Outline each Plasmodium parasite.
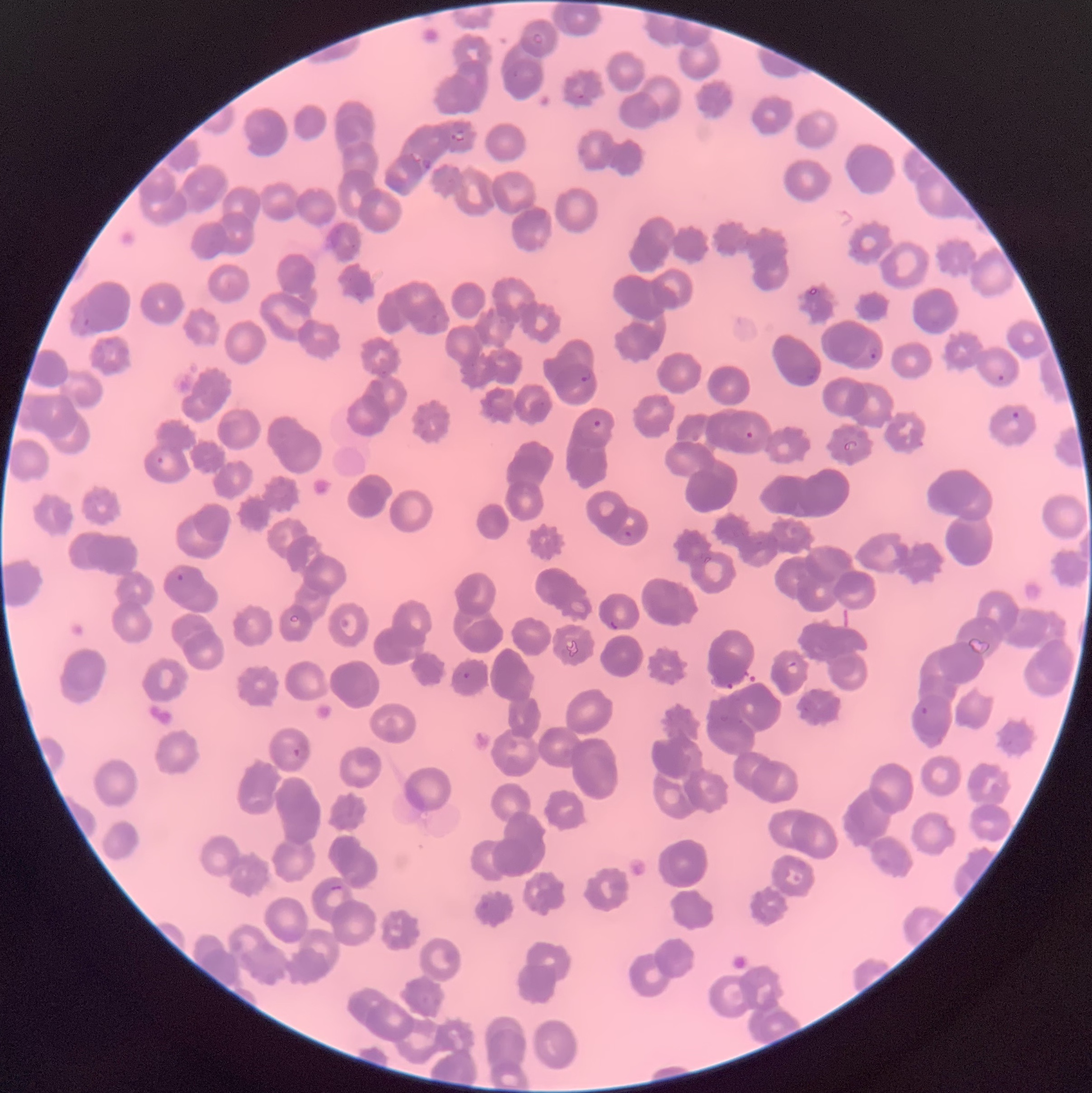
Approximate bounding boxes as named x1/y1/x2/y2 corners in pixels.
Plasmodium parasites: (x1=532, y1=32, x2=544, y2=45), (x1=512, y1=69, x2=519, y2=79), (x1=572, y1=88, x2=584, y2=99), (x1=450, y1=129, x2=467, y2=142), (x1=421, y1=158, x2=434, y2=169), (x1=73, y1=317, x2=90, y2=336), (x1=866, y1=338, x2=880, y2=362), (x1=806, y1=364, x2=819, y2=382), (x1=579, y1=370, x2=595, y2=382), (x1=997, y1=374, x2=1005, y2=381), (x1=1011, y1=410, x2=1020, y2=419), (x1=594, y1=420, x2=602, y2=428), (x1=742, y1=429, x2=754, y2=439), (x1=843, y1=439, x2=859, y2=451), (x1=156, y1=456, x2=165, y2=466), (x1=623, y1=529, x2=633, y2=544), (x1=175, y1=573, x2=184, y2=582), (x1=608, y1=618, x2=621, y2=630), (x1=786, y1=662, x2=799, y2=675), (x1=461, y1=671, x2=470, y2=680), (x1=920, y1=707, x2=928, y2=714), (x1=290, y1=743, x2=309, y2=760), (x1=330, y1=886, x2=344, y2=890).

Summary:
  - Red blood cell morphology: rouleaux formation
  - Modality: optical microscopy
  - Preparation: thin blood smear
  - Image size: 1092×1093 pixels